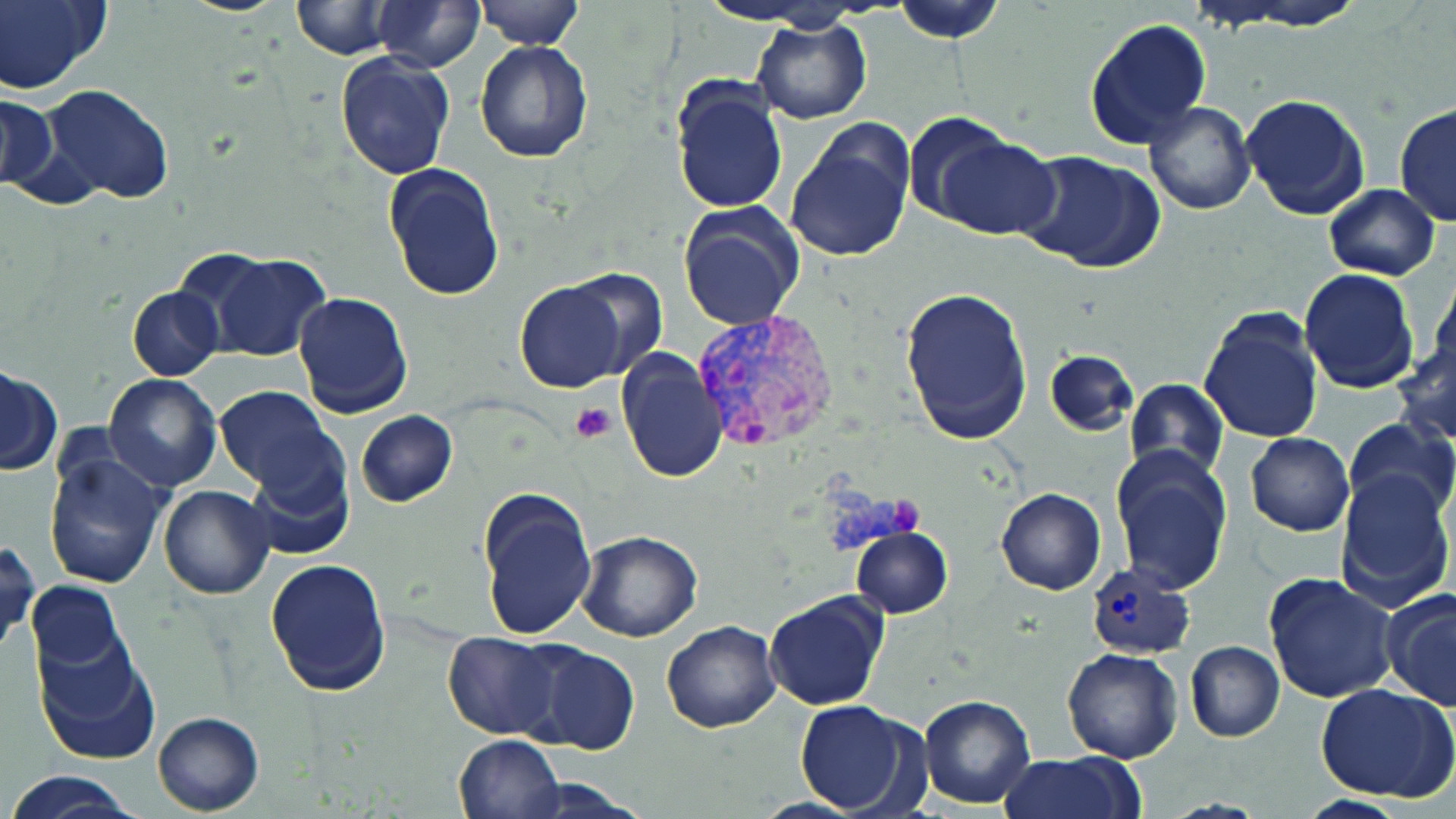
slide-level diagnosis = Plasmodium vivax
stain = May-Grünwald-Giemsa
platelet locations = approximate bounding boxes as (x1,y1)-(x2,y2) corner pairs in pixels: (572,403)-(616,442)
uninfected red blood cell locations = approximate bounding boxes as (x1,y1)-(x2,y2) corner pairs in pixels: (0,0)-(109,93), (175,0)-(291,17), (476,0)-(581,49), (894,0)-(1006,43), (290,1)-(397,58), (374,1)-(483,70), (1218,2)-(1372,31), (751,18)-(871,123), (1084,18)-(1212,149), (474,40)-(595,164), (333,48)-(455,177), (671,78)-(788,215), (40,86)-(177,205), (1,92)-(59,194), (1238,93)-(1369,221), (1144,101)-(1254,215), (1395,103)-(1456,230), (784,120)-(916,264), (921,133)-(1062,240), (1015,150)-(1166,274), (383,163)-(505,302), (1323,184)-(1440,280), (678,201)-(805,331), (186,248)-(331,362), (1297,268)-(1419,394), (558,269)-(669,382), (1428,271)-(1456,378), (514,279)-(628,393), (900,284)-(1032,447), (127,285)-(224,380), (291,291)-(413,419), (1199,306)-(1324,448), (1393,335)-(1456,448), (615,349)-(728,484), (1045,349)-(1137,437), (1,365)-(63,476), (103,374)-(224,492), (1125,378)-(1230,482), (212,386)-(345,500), (355,410)-(457,507), (1341,418)-(1455,522), (1246,432)-(1355,537), (44,442)-(170,593), (240,445)-(354,560), (1109,445)-(1233,596), (1333,469)-(1453,609), (159,485)-(275,599), (477,488)-(597,641), (996,489)-(1106,595), (851,526)-(953,618), (576,530)-(705,642), (1,541)-(37,653), (266,558)-(392,696), (1265,570)-(1400,704), (27,580)-(127,676), (1380,589)-(1456,710), (763,590)-(891,713), (661,620)-(782,733), (33,633)-(161,766), (442,633)-(562,739), (508,638)-(643,755), (1184,641)-(1284,742), (1061,648)-(1183,764), (1316,683)-(1456,802), (919,693)-(1036,808), (793,698)-(929,816), (152,711)-(264,815), (453,734)-(563,819), (999,750)-(1144,818), (5,769)-(143,819), (509,774)-(650,818)
magnification = 1000x
field of view = single
modality = optical microscopy
image size = 1456×819 pixels
Plasmodium vivax-infected red blood cell locations = approximate bounding boxes as (x1,y1)-(x2,y2) corner pairs in pixels: (691,309)-(840,452), (1084,563)-(1196,659)
preparation = thin blood film